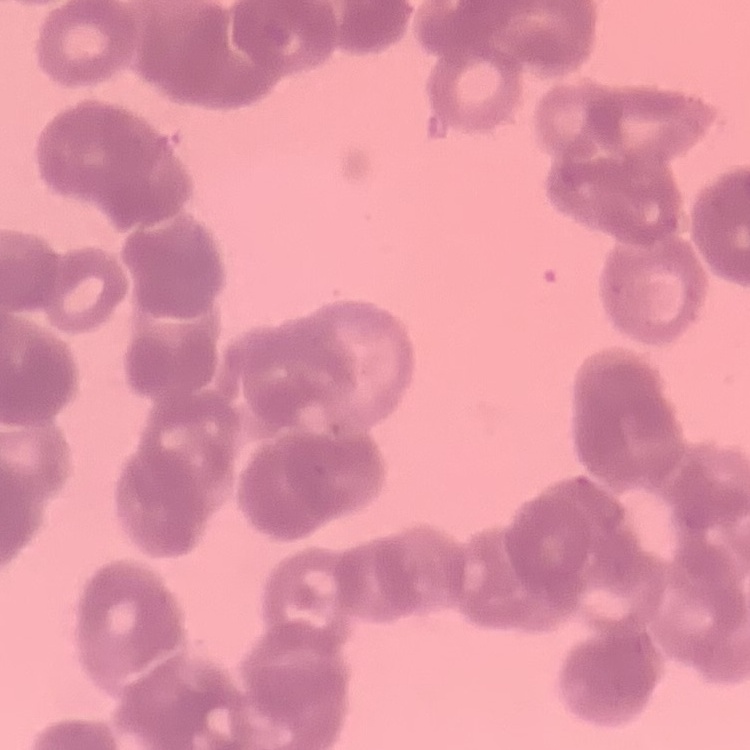
Summary:
  - Red blood cell morphology: rouleaux formation
  - Image type: one tile cut from a larger photomicrograph
  - Stain: Field's or Giemsa
  - Preparation: thin blood smear